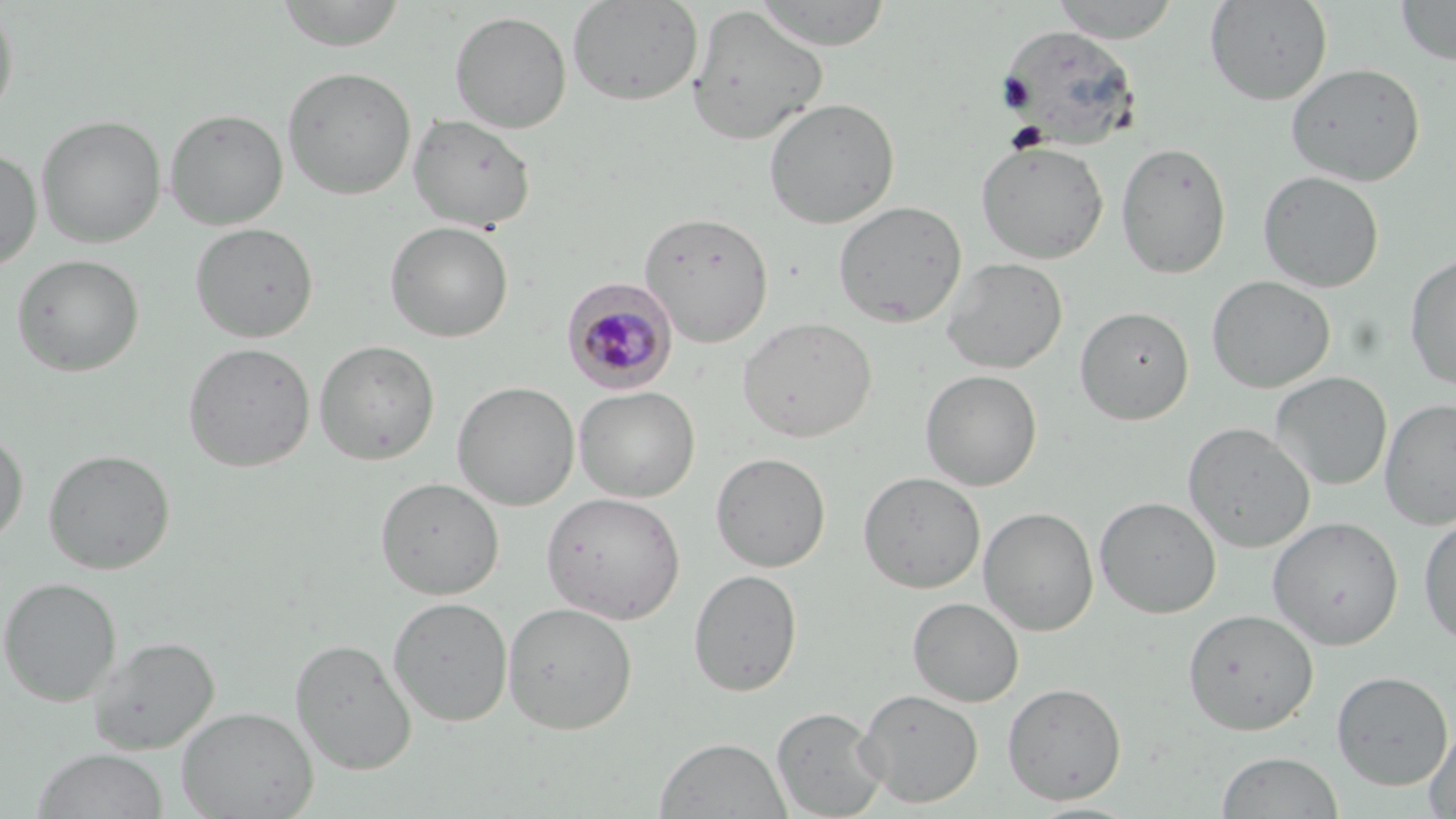

{
  "plasmodium_malariae_infected_red_blood_cell_locations": "approximate bounding boxes as (x1,y1)-(x2,y2) corner pairs in pixels: (561,277)-(678,394)",
  "slide_level_diagnosis": "Plasmodium malariae",
  "preparation": "thin blood smear",
  "stain": "May-Grünwald-Giemsa",
  "magnification": "1000x",
  "field_of_view": "single",
  "image_size": "1456×819 pixels",
  "modality": "light microscopy",
  "uninfected_red_blood_cell_locations": "approximate bounding boxes as (x1,y1)-(x2,y2) corner pairs in pixels: (273,0)-(407,52), (752,0)-(893,50), (1049,0)-(1183,42), (1205,0)-(1332,105), (1395,0)-(1456,65), (567,1)-(703,106), (0,2)-(20,126), (686,5)-(828,146), (449,10)-(572,133), (996,23)-(1140,149), (1285,62)-(1425,185), (281,65)-(417,199), (763,97)-(900,229), (164,108)-(288,230), (179,108)-(300,341), (408,113)-(536,232), (36,114)-(166,248), (976,140)-(1109,263), (1116,141)-(1232,280), (0,146)-(42,272), (1257,170)-(1384,293), (833,200)-(967,327), (638,210)-(774,347), (385,221)-(513,342), (190,222)-(318,343), (1404,251)-(1456,390), (11,254)-(144,376), (941,257)-(1067,374), (1207,275)-(1335,393), (1075,305)-(1194,424), (737,316)-(877,442), (314,339)-(440,465), (182,341)-(316,472), (921,368)-(1042,491), (1270,371)-(1392,490), (452,381)-(580,511), (574,386)-(700,502), (1380,398)-(1456,530), (1183,422)-(1316,553), (0,426)-(29,548), (43,448)-(176,574), (711,452)-(831,573), (858,470)-(986,593), (375,476)-(505,599), (541,491)-(686,624), (1094,496)-(1221,618), (979,507)-(1098,636), (1418,511)-(1456,646), (1267,516)-(1404,650), (689,568)-(803,696), (0,576)-(122,706), (387,596)-(513,725), (907,597)-(1024,707), (502,601)-(637,734), (1182,608)-(1319,735), (89,636)-(219,754), (290,638)-(417,775), (1331,670)-(1453,790), (1002,681)-(1127,804), (856,688)-(984,808), (177,706)-(318,819), (771,706)-(887,818), (1423,719)-(1456,818), (655,736)-(791,818), (31,747)-(169,819), (1215,750)-(1344,819), (1025,800)-(1145,819)"
}